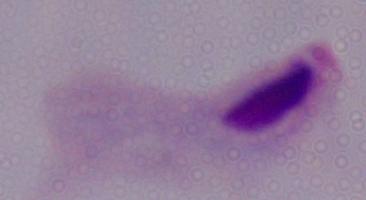
modality = photomicrograph
magnification = 1000x
identification = trichomonad